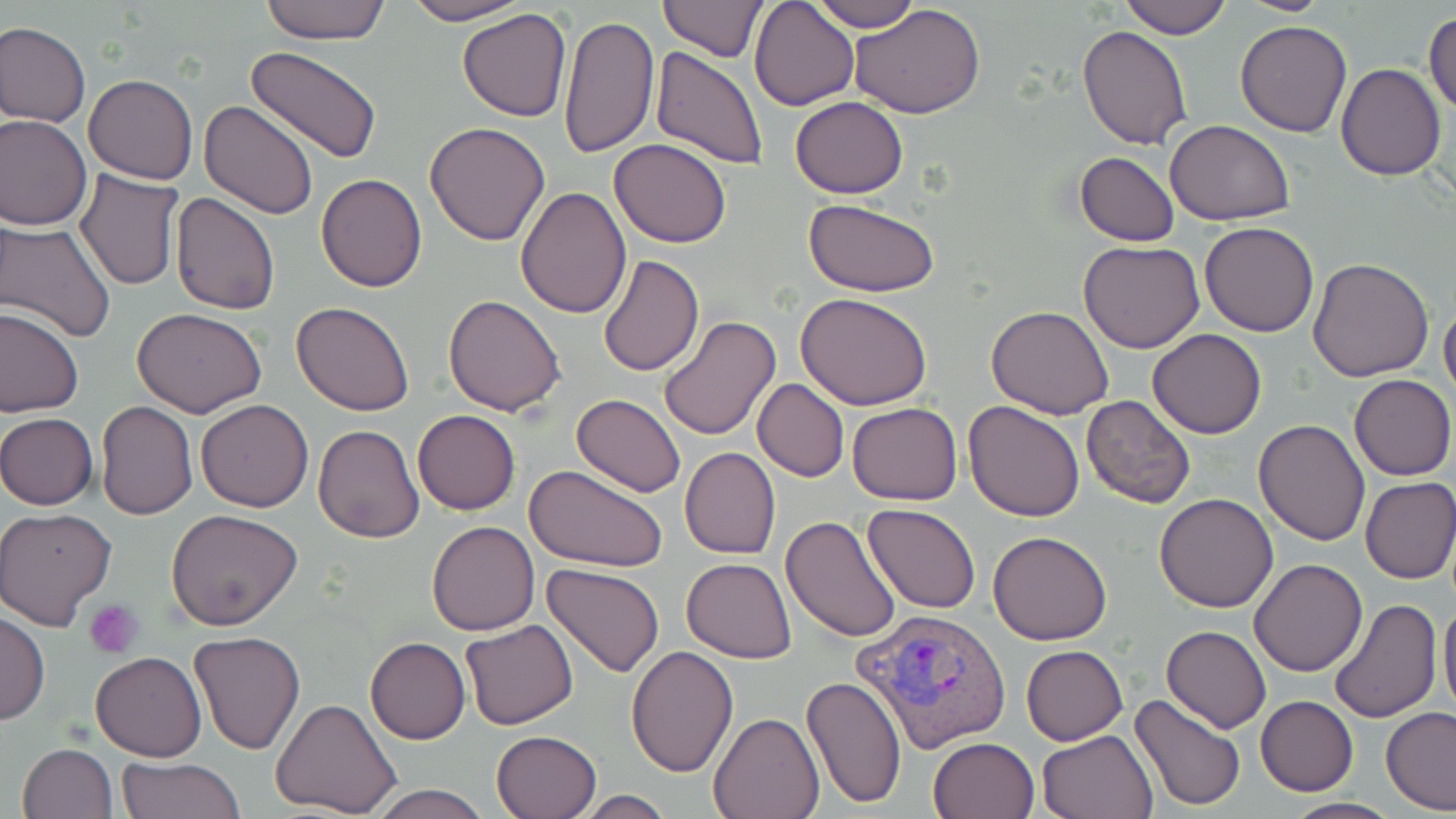

slide_level_diagnosis: Plasmodium vivax
modality: light microscopy
platelet_locations: 'approximate bounding boxes as (x1, y1, x2, y2) in pixels: (85, 597, 143, 657)'
field_of_view: one of a larger specimen
uninfected_red_blood_cell_locations: 'approximate bounding boxes as (x1, y1, x2, y2) in pixels: (258, 0, 394, 43), (398, 0, 534, 25), (657, 0, 767, 61), (751, 0, 860, 111), (807, 0, 922, 32), (1117, 0, 1232, 40), (1235, 0, 1337, 16), (850, 4, 987, 117), (458, 8, 572, 122), (1423, 8, 1456, 120), (558, 14, 660, 160), (1235, 19, 1352, 137), (0, 22, 91, 128), (1077, 27, 1193, 149), (247, 45, 382, 164), (649, 47, 769, 170), (1336, 64, 1447, 182), (83, 74, 198, 184), (790, 97, 908, 198), (200, 99, 321, 220), (0, 113, 93, 230), (1163, 119, 1296, 225), (424, 121, 550, 246), (610, 138, 731, 247), (1075, 151, 1181, 246), (75, 169, 184, 291), (316, 174, 427, 293), (515, 186, 632, 318), (170, 193, 280, 316), (803, 199, 938, 297), (0, 217, 118, 344), (1200, 221, 1319, 337), (1078, 239, 1204, 352), (599, 254, 704, 375), (1308, 257, 1435, 381), (794, 291, 934, 410), (443, 293, 566, 416), (1439, 298, 1456, 406), (292, 302, 416, 417), (986, 305, 1114, 420), (0, 308, 83, 418), (133, 308, 267, 419), (659, 316, 782, 442), (1147, 329, 1267, 438), (1350, 373, 1455, 481), (752, 379, 849, 481), (571, 393, 687, 497), (1081, 394, 1196, 509), (195, 399, 314, 512), (95, 400, 198, 520), (964, 400, 1084, 521), (847, 401, 963, 505), (413, 409, 521, 516), (0, 412, 100, 511), (1254, 418, 1370, 546), (313, 425, 424, 544), (679, 447, 780, 559), (525, 464, 667, 571), (1359, 476, 1456, 584), (1153, 493, 1278, 612), (863, 504, 981, 614), (166, 507, 304, 630), (1, 508, 118, 630), (782, 514, 904, 643), (427, 521, 540, 635), (988, 529, 1113, 645), (681, 557, 797, 663), (1249, 558, 1367, 676), (542, 563, 667, 678), (1438, 590, 1456, 722), (1329, 598, 1441, 724), (0, 610, 49, 725), (459, 619, 579, 730), (1160, 625, 1271, 733), (190, 631, 306, 754), (365, 637, 471, 744), (1021, 645, 1128, 745), (626, 646, 738, 778), (91, 650, 207, 761), (800, 674, 906, 810), (1129, 693, 1247, 813), (1255, 695, 1359, 796), (271, 698, 402, 819), (1380, 706, 1456, 814), (709, 712, 823, 819), (1038, 728, 1159, 819), (492, 730, 600, 818), (929, 737, 1039, 819), (18, 743, 118, 819), (115, 757, 244, 819), (365, 783, 495, 819), (573, 790, 675, 819), (1281, 796, 1400, 818)'
preparation: thin blood film
stain: May-Grünwald-Giemsa
image_size: 1456×819 pixels
magnification: 1000x
plasmodium_vivax_infected_red_blood_cell_locations: 'approximate bounding boxes as (x1, y1, x2, y2) in pixels: (854, 606, 1012, 752)'